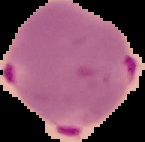
Summary:
  - Image size: 145×142 pixels
  - Preparation: thin blood smear
  - Image type: segmented cell region on a black background
  - Result: Plasmodium parasites identified